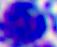

modality = micrograph
identification = white blood cell
magnification = 400x